Comment on the morphology of the erythrocytes.
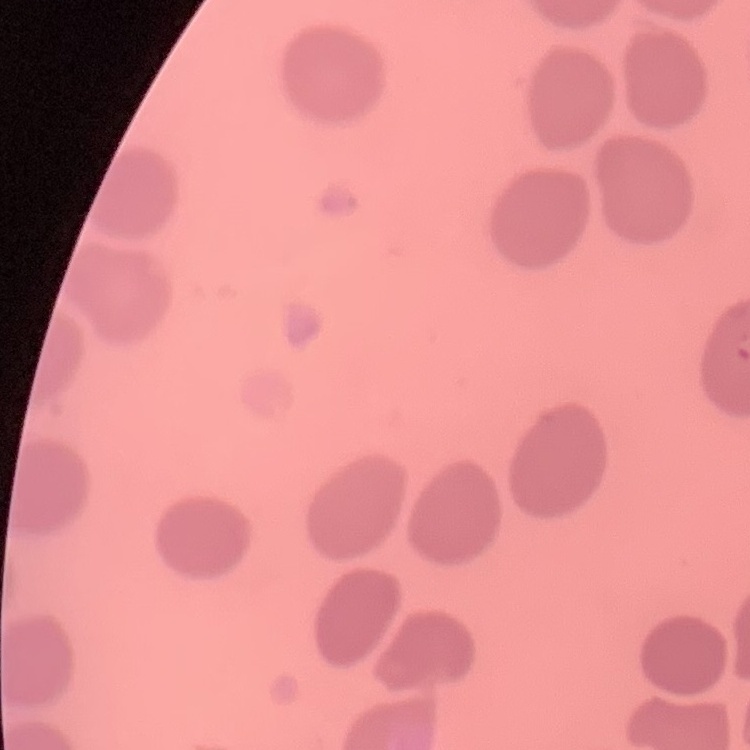

No rouleaux formation.

Summary:
  - Preparation: thin peripheral smear
  - Image type: square crop of a larger photomicrograph
  - Stain: Field's or Giemsa